Outline platelets.
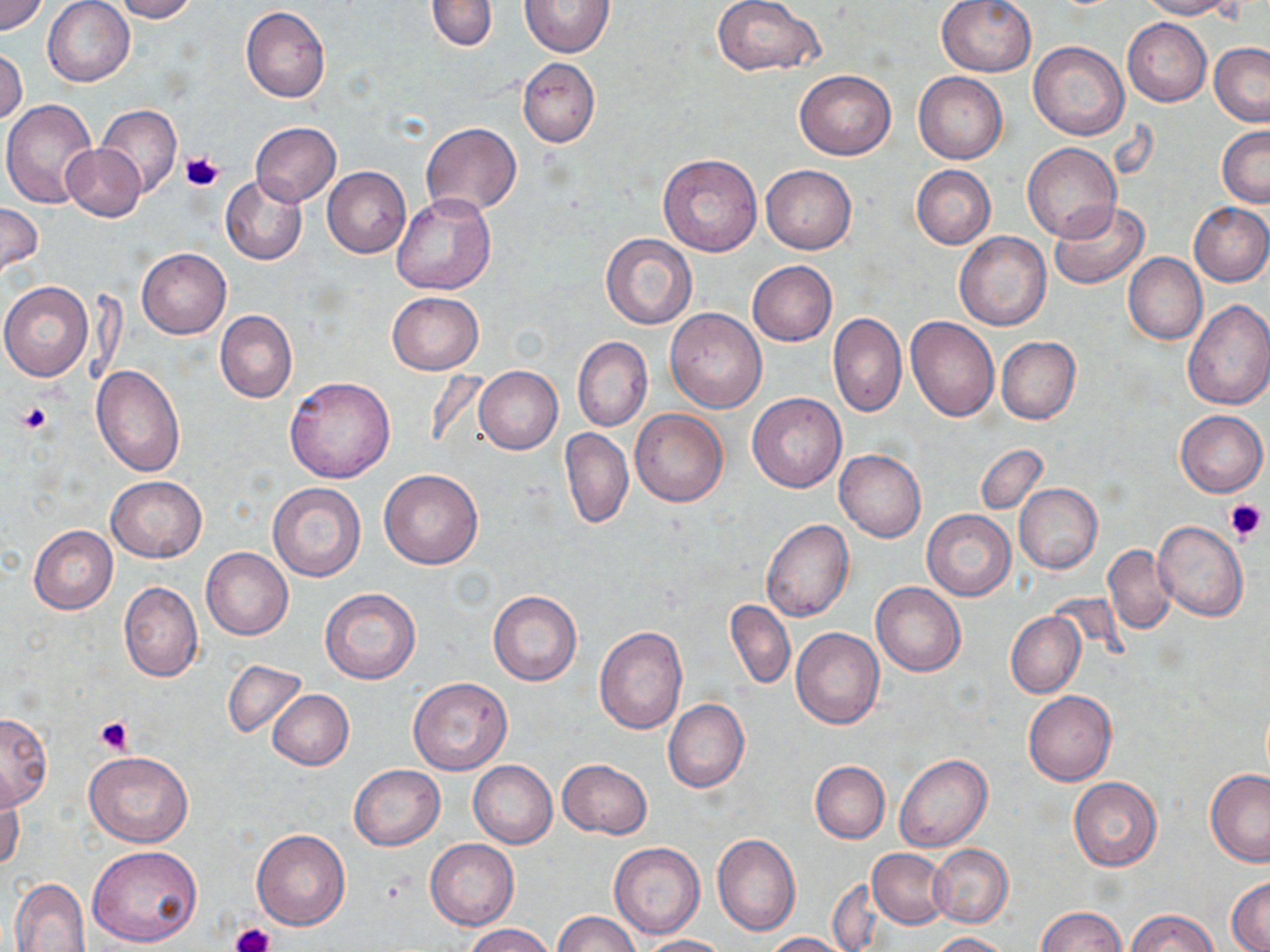
Approximate bounding boxes as (x1, y1, x2, y2) in pixels.
Platelets: (180, 149, 225, 191), (16, 401, 54, 435), (1224, 496, 1267, 541), (96, 716, 132, 755), (233, 924, 271, 952).

slide-level diagnosis = negative for blood parasites
stain = May-Grünwald-Giemsa
magnification = 1000x
image size = 1270×952 pixels
uninfected red blood cell locations = approximate bounding boxes as (x1, y1, x2, y2) in pixels: (0, 0, 48, 36), (110, 0, 198, 21), (426, 0, 498, 52), (519, 0, 614, 58), (711, 0, 825, 76), (936, 0, 1037, 76), (1135, 0, 1238, 19), (44, 1, 135, 86), (241, 7, 330, 102), (1122, 17, 1211, 106), (1028, 42, 1128, 140), (1209, 43, 1270, 126), (1, 48, 27, 127), (518, 57, 600, 147), (795, 69, 897, 160), (913, 72, 1007, 163), (3, 100, 100, 209), (96, 105, 181, 199), (250, 121, 340, 206), (422, 122, 522, 215), (1217, 125, 1270, 208), (1022, 142, 1122, 243), (60, 144, 144, 220), (657, 153, 761, 255), (761, 164, 856, 254), (911, 165, 995, 249), (323, 167, 410, 257), (220, 175, 307, 265), (391, 195, 495, 295), (1050, 200, 1148, 289), (0, 201, 43, 279), (1189, 201, 1270, 286), (955, 232, 1051, 331), (601, 234, 696, 329), (137, 248, 231, 338), (1123, 252, 1207, 345), (748, 261, 836, 346), (0, 281, 93, 381), (386, 292, 483, 374), (1181, 299, 1270, 410), (664, 308, 768, 412), (215, 310, 297, 403), (827, 313, 906, 417), (906, 316, 999, 421), (996, 336, 1080, 423), (573, 337, 651, 432), (90, 365, 184, 477), (473, 367, 562, 453), (285, 376, 395, 482), (747, 392, 846, 492), (630, 408, 727, 507), (1175, 409, 1267, 497), (560, 427, 633, 529), (976, 443, 1047, 516), (834, 449, 925, 542), (379, 469, 483, 569), (106, 475, 206, 562), (268, 483, 365, 582), (1014, 484, 1102, 572), (922, 509, 1015, 600), (761, 519, 854, 622), (1152, 521, 1248, 622), (29, 525, 117, 614), (1103, 545, 1176, 634), (201, 547, 293, 639), (119, 581, 202, 681), (870, 583, 965, 676), (321, 589, 421, 684), (488, 591, 582, 686), (725, 598, 795, 690), (1005, 611, 1085, 698), (594, 627, 687, 733), (791, 627, 883, 729), (222, 659, 307, 738), (407, 677, 512, 775), (268, 689, 354, 769), (1023, 689, 1117, 786), (662, 699, 749, 793), (0, 711, 52, 807), (84, 751, 192, 847), (894, 753, 992, 853), (558, 759, 652, 839), (468, 760, 557, 848), (811, 760, 889, 843), (350, 764, 444, 850), (1205, 769, 1270, 866), (0, 772, 23, 873), (1068, 777, 1162, 871), (251, 829, 351, 930), (712, 834, 800, 935), (425, 839, 518, 929), (609, 842, 705, 939), (89, 845, 202, 947), (929, 845, 1012, 927), (868, 849, 952, 927), (1227, 876, 1270, 952), (9, 877, 93, 952), (828, 880, 885, 950), (1037, 906, 1126, 952), (1125, 909, 1218, 952), (553, 912, 641, 952), (463, 924, 554, 952), (764, 932, 848, 951), (929, 932, 1015, 952), (639, 935, 726, 951)
modality = light microscopy
preparation = thin blood smear
field of view = one of a larger specimen